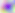 400x magnification. Toxoplasma gondii is seen. Micrograph.